Give the position of every leukocyte visible.
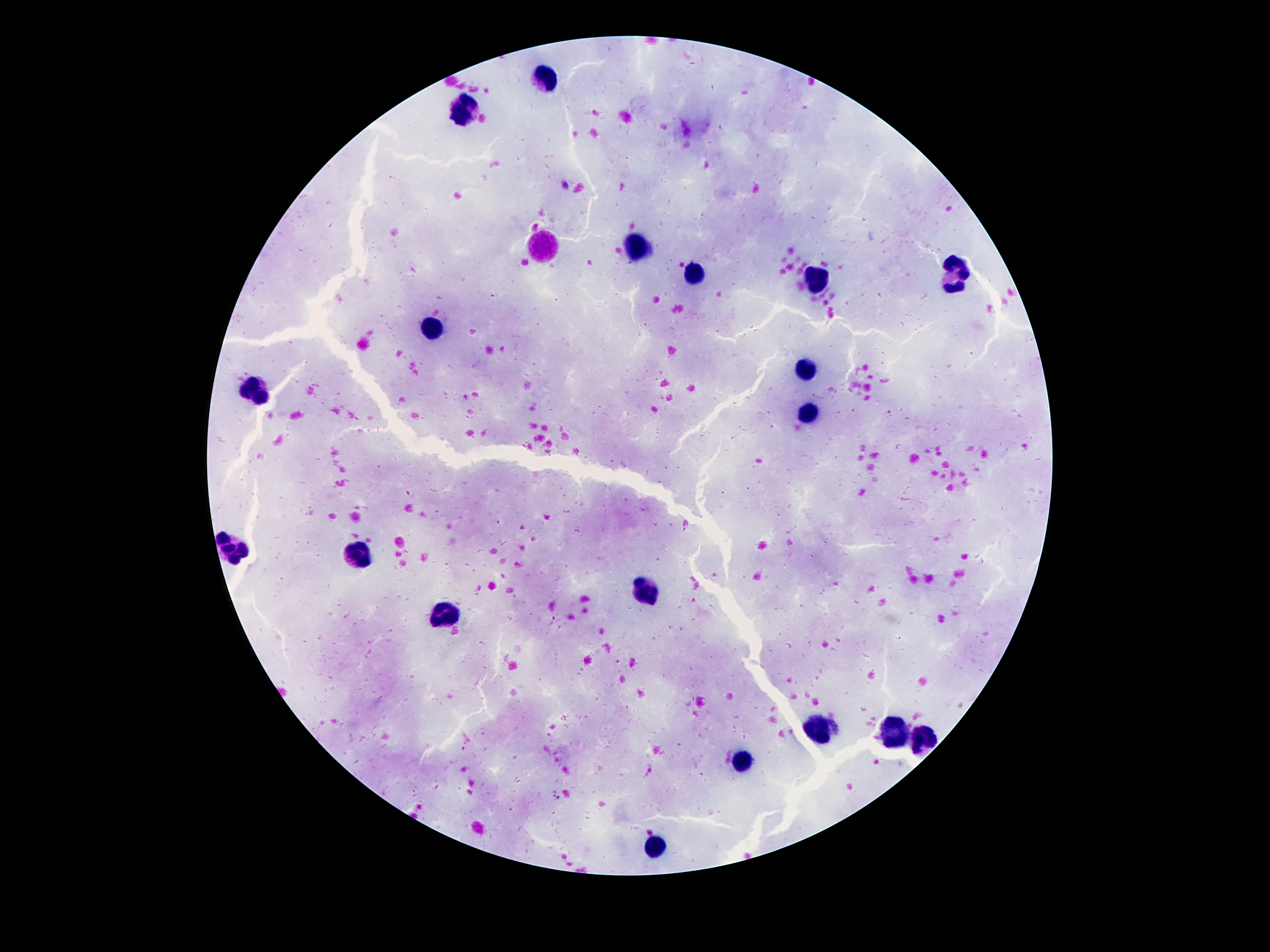

Approximate object centers, in pixels from the top-left corner.
Leukocytes: (x=541, y=76), (x=465, y=111), (x=637, y=244), (x=955, y=271), (x=691, y=277), (x=816, y=283), (x=430, y=324), (x=807, y=367), (x=258, y=387), (x=807, y=414), (x=227, y=549), (x=355, y=556), (x=644, y=589), (x=447, y=615), (x=820, y=728), (x=894, y=732), (x=924, y=740), (x=742, y=760), (x=656, y=847).

One field from this slide. Patient malaria status: not infected. Giemsa stain. Thick peripheral-blood smear. Image is 1270×952 pixels. Photographed through the microscope eyepiece with a smartphone camera. 100x magnification.